Report the malaria status of this cell.
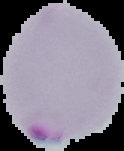

It is parasitized.

image type = cell region segmented out of the field of view; surrounding area masked to black
image size = 124×151 pixels
preparation = thin blood smear